Classify this cell by malaria status.
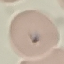
It is uninfected.

{
  "stain": "Giemsa",
  "preparation": "thin blood film",
  "image_type": "cell patch, automatically extracted from a larger field of view and resized to 64 × 64 pixels",
  "capture": "smartphone through the microscope eyepiece"
}